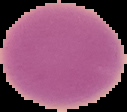

malaria status = uninfected
image size = 127×112 pixels
image type = cell region segmented out of the field of view; surrounding area masked to black
preparation = thin blood film